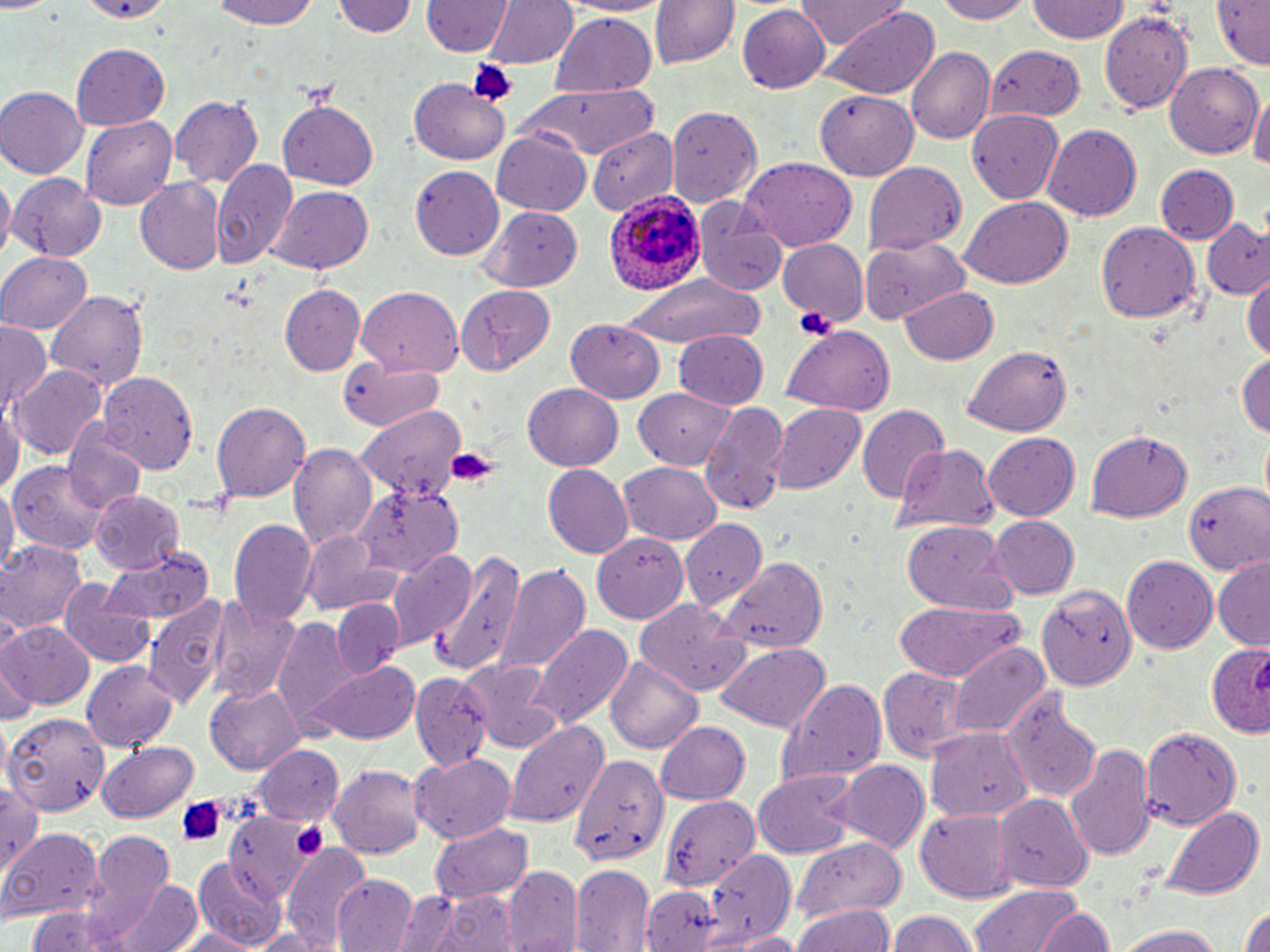

Summary:
  - Coordinate format: approximate bounding boxes as [x1, y1, x2, y2] in pixels
  - Platelet locations: [466, 58, 515, 106], [797, 306, 836, 341], [432, 445, 501, 497], [175, 795, 226, 845], [289, 820, 329, 863]
  - Plasmodium ovale-infected red blood cell locations: [605, 191, 705, 295]
  - Uninfected red blood cell locations: [79, 0, 171, 23], [206, 0, 327, 29], [336, 0, 417, 39], [482, 0, 577, 70], [557, 0, 670, 19], [650, 0, 739, 69], [796, 0, 907, 50], [927, 0, 1034, 24], [1024, 0, 1130, 43], [1208, 0, 1269, 67], [423, 1, 509, 58], [0, 2, 54, 16], [738, 2, 832, 91], [1099, 7, 1196, 111], [828, 9, 940, 99], [548, 14, 658, 95], [69, 45, 168, 129], [905, 46, 996, 143], [986, 47, 1087, 121], [1163, 60, 1262, 158], [408, 78, 511, 165], [512, 83, 659, 159], [0, 88, 87, 179], [816, 90, 919, 180], [1250, 93, 1270, 180], [171, 95, 264, 192], [278, 98, 377, 189], [666, 103, 761, 203], [964, 108, 1066, 206], [81, 115, 178, 208], [1043, 126, 1140, 221], [586, 127, 678, 216], [493, 131, 592, 215], [740, 157, 857, 249], [210, 159, 297, 270], [864, 162, 967, 258], [1155, 164, 1237, 243], [412, 165, 504, 260], [8, 173, 106, 261], [0, 178, 14, 259], [136, 178, 225, 275], [265, 185, 376, 274], [959, 197, 1074, 288], [698, 200, 785, 298], [478, 205, 584, 291], [1203, 221, 1270, 301], [1094, 222, 1200, 323], [862, 235, 968, 323], [775, 238, 865, 334], [776, 239, 867, 325], [0, 252, 92, 336], [617, 270, 763, 349], [1244, 278, 1270, 362], [280, 284, 364, 374], [455, 285, 557, 372], [356, 287, 466, 375], [899, 287, 1000, 364], [45, 290, 150, 395], [564, 319, 662, 401], [0, 321, 52, 409], [779, 327, 896, 414], [674, 328, 770, 408], [964, 346, 1072, 436], [1236, 351, 1270, 440], [339, 360, 448, 433], [11, 362, 106, 459], [97, 373, 199, 473], [521, 383, 625, 470], [633, 391, 735, 469], [212, 399, 311, 500], [698, 399, 789, 514], [0, 402, 21, 504], [767, 403, 867, 495], [357, 407, 466, 501], [859, 407, 948, 504], [64, 426, 146, 516], [1087, 430, 1192, 521], [983, 433, 1082, 522], [1259, 433, 1269, 512], [288, 442, 379, 555], [892, 442, 1000, 533], [9, 458, 112, 555], [618, 460, 722, 545], [543, 464, 634, 558], [1184, 481, 1270, 574], [0, 483, 16, 581], [353, 485, 462, 575], [90, 489, 184, 576], [680, 517, 768, 611], [989, 517, 1079, 599], [230, 518, 316, 626], [900, 520, 1014, 614], [591, 530, 691, 623], [0, 539, 88, 636], [300, 543, 408, 617], [101, 545, 215, 626], [390, 549, 476, 649], [429, 553, 528, 676], [1122, 555, 1218, 655], [718, 557, 828, 651], [1213, 557, 1270, 648], [496, 562, 590, 677], [62, 577, 152, 666], [1036, 579, 1140, 691], [207, 594, 299, 706], [145, 595, 229, 711], [894, 599, 1025, 681], [334, 601, 404, 677], [637, 603, 751, 697], [273, 616, 355, 732], [1, 621, 95, 711], [532, 625, 633, 729], [1207, 641, 1270, 736], [948, 642, 1050, 739], [714, 643, 830, 732], [608, 656, 704, 752], [461, 658, 565, 750], [84, 661, 178, 753], [306, 662, 420, 743], [1, 665, 36, 725], [877, 668, 966, 763], [409, 673, 489, 770], [778, 678, 887, 786], [202, 687, 303, 776], [1002, 687, 1103, 804], [5, 707, 109, 813], [654, 719, 753, 805], [503, 721, 611, 825], [1138, 724, 1240, 832], [927, 729, 1031, 822], [1067, 743, 1156, 862], [95, 744, 199, 822], [253, 746, 345, 824], [411, 753, 518, 842], [563, 755, 666, 886], [830, 762, 929, 854], [328, 763, 427, 857], [752, 771, 854, 857], [0, 778, 43, 880], [658, 792, 760, 892], [995, 793, 1092, 890], [1158, 807, 1263, 901], [915, 808, 1016, 902], [221, 814, 313, 896], [430, 823, 534, 905], [2, 830, 101, 923], [88, 832, 175, 924], [793, 836, 906, 919], [283, 845, 372, 951], [707, 849, 797, 944], [193, 858, 288, 947], [570, 864, 656, 951], [504, 866, 580, 952], [333, 875, 417, 952], [111, 879, 204, 952], [639, 884, 715, 950], [971, 884, 1083, 952], [396, 888, 476, 950], [432, 889, 517, 952], [794, 903, 894, 952], [1238, 904, 1270, 952], [1033, 905, 1116, 952], [23, 907, 136, 952], [886, 910, 981, 952], [1111, 920, 1231, 951], [247, 926, 326, 950], [171, 927, 262, 952], [732, 931, 807, 952]
  - Slide-level diagnosis: Plasmodium ovale
  - Magnification: 1000x
  - Preparation: thin blood film
  - Modality: light microscopy
  - Image size: 1270×952 pixels
  - Stain: May-Grünwald-Giemsa
  - Field of view: single